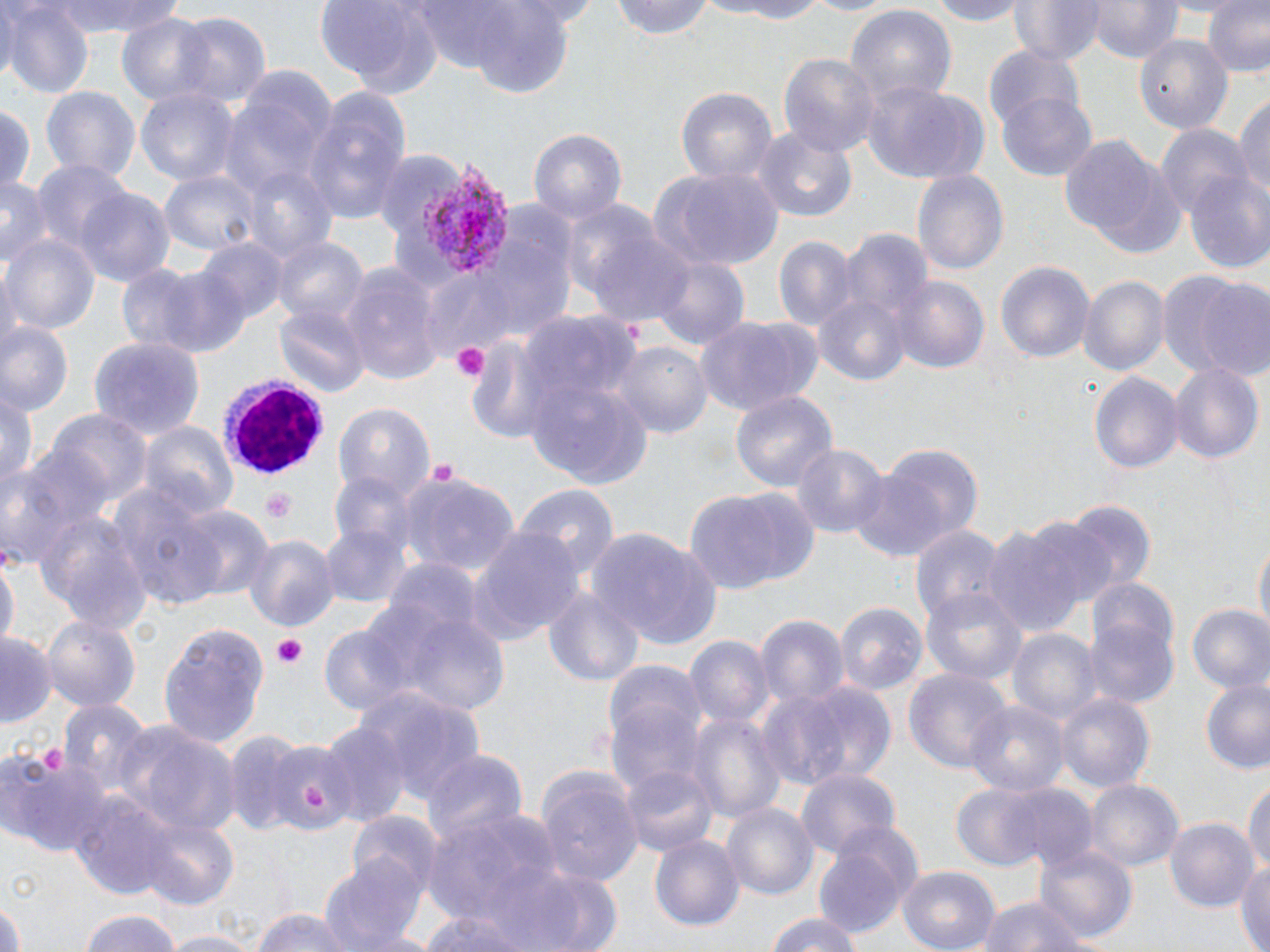

Summary:
  - Coordinate format: approximate bounding boxes as [x1, y1, x2, y2] in pixels
  - Uninfected red blood cell locations: [43, 0, 184, 36], [608, 0, 716, 42], [700, 0, 838, 24], [795, 0, 900, 17], [917, 0, 1035, 25], [1013, 0, 1104, 67], [1090, 0, 1180, 64], [1200, 0, 1270, 78], [314, 1, 441, 93], [0, 2, 93, 97], [408, 2, 583, 89], [846, 5, 955, 111], [115, 13, 218, 109], [172, 13, 273, 107], [1138, 37, 1226, 129], [984, 45, 1087, 137], [779, 52, 881, 161], [861, 81, 990, 185], [39, 86, 141, 189], [135, 86, 239, 189], [302, 87, 410, 222], [676, 87, 778, 191], [997, 90, 1099, 180], [1233, 95, 1270, 205], [215, 99, 321, 198], [1, 102, 36, 196], [1156, 125, 1248, 219], [527, 128, 628, 226], [752, 128, 857, 222], [1057, 132, 1179, 255], [32, 163, 134, 264], [243, 167, 336, 265], [161, 168, 261, 258], [647, 168, 784, 270], [913, 170, 1009, 275], [1184, 173, 1270, 273], [0, 175, 49, 270], [74, 187, 176, 286], [561, 200, 661, 302], [480, 213, 580, 344], [838, 227, 933, 334], [587, 229, 696, 328], [4, 233, 100, 336], [773, 235, 861, 333], [272, 237, 368, 328], [199, 239, 287, 324], [650, 255, 751, 352], [994, 259, 1096, 367], [119, 261, 250, 357], [342, 261, 442, 386], [1162, 272, 1268, 382], [1079, 275, 1168, 379], [893, 277, 989, 376], [812, 292, 910, 387], [276, 304, 369, 399], [519, 310, 637, 418], [694, 315, 824, 417], [2, 323, 74, 415], [91, 335, 204, 441], [464, 337, 561, 443], [613, 342, 712, 443], [1168, 360, 1263, 465], [1089, 370, 1183, 479], [528, 379, 654, 487], [1, 386, 38, 494], [730, 389, 839, 494], [332, 402, 434, 503], [50, 410, 151, 510], [137, 421, 239, 520], [792, 444, 887, 539], [880, 444, 984, 542], [0, 452, 102, 568], [846, 468, 951, 562], [397, 476, 519, 576], [113, 483, 230, 608], [512, 486, 617, 585], [685, 486, 820, 595], [1062, 502, 1156, 598], [179, 504, 274, 601], [40, 512, 148, 633], [981, 521, 1098, 641], [907, 522, 1008, 625], [322, 523, 409, 609], [468, 529, 583, 641], [594, 531, 725, 651], [245, 533, 339, 633], [1253, 536, 1269, 636], [0, 554, 17, 654], [383, 558, 485, 642], [1085, 578, 1181, 676], [544, 586, 644, 690], [923, 586, 1028, 686], [362, 596, 509, 713], [834, 598, 927, 697], [1185, 604, 1270, 694], [41, 613, 140, 716], [754, 613, 849, 707], [1086, 617, 1180, 712], [317, 619, 420, 719], [160, 624, 269, 749], [1008, 628, 1102, 730], [684, 632, 774, 730], [0, 633, 54, 724], [600, 656, 711, 797], [902, 665, 1013, 775], [1198, 676, 1270, 776], [763, 679, 897, 789], [356, 687, 485, 801], [1054, 692, 1156, 798], [57, 699, 153, 789], [967, 699, 1069, 796], [691, 712, 784, 826], [321, 719, 410, 826], [114, 722, 239, 836], [271, 740, 348, 830], [421, 750, 528, 852], [2, 752, 109, 856], [618, 760, 719, 860], [796, 768, 898, 861], [533, 771, 643, 888], [1084, 778, 1184, 872], [1244, 778, 1270, 880], [951, 782, 1063, 871], [69, 789, 185, 898], [721, 802, 817, 903], [424, 804, 567, 927], [347, 812, 443, 903], [139, 817, 239, 909], [835, 818, 922, 899], [1167, 818, 1259, 913], [650, 833, 743, 933], [1036, 845, 1136, 945], [813, 847, 907, 939], [320, 853, 429, 952], [1234, 857, 1270, 951], [898, 867, 1000, 952], [524, 871, 623, 952], [974, 896, 1089, 952], [0, 900, 29, 952], [417, 905, 545, 952], [248, 908, 357, 952], [76, 909, 184, 952], [762, 911, 862, 952], [163, 931, 252, 952]
  - Plasmodium vivax-infected red blood cell locations: [418, 160, 510, 279]
  - White blood cell locations: [222, 379, 329, 475]
  - Platelet locations: [450, 341, 488, 382], [428, 458, 460, 486], [260, 488, 299, 522], [272, 634, 307, 670], [302, 783, 329, 810]
  - Slide-level diagnosis: Plasmodium vivax
  - Image size: 1270×952 pixels
  - Modality: optical microscopy
  - Field of view: one of a larger specimen
  - Stain: May-Grünwald-Giemsa
  - Preparation: thin blood smear
  - Magnification: 1000x